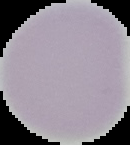
result: negative for Plasmodium parasites
preparation: thin blood film
image_size: 130×145 pixels
image_type: cell region segmented out of the field of view; surrounding area masked to black